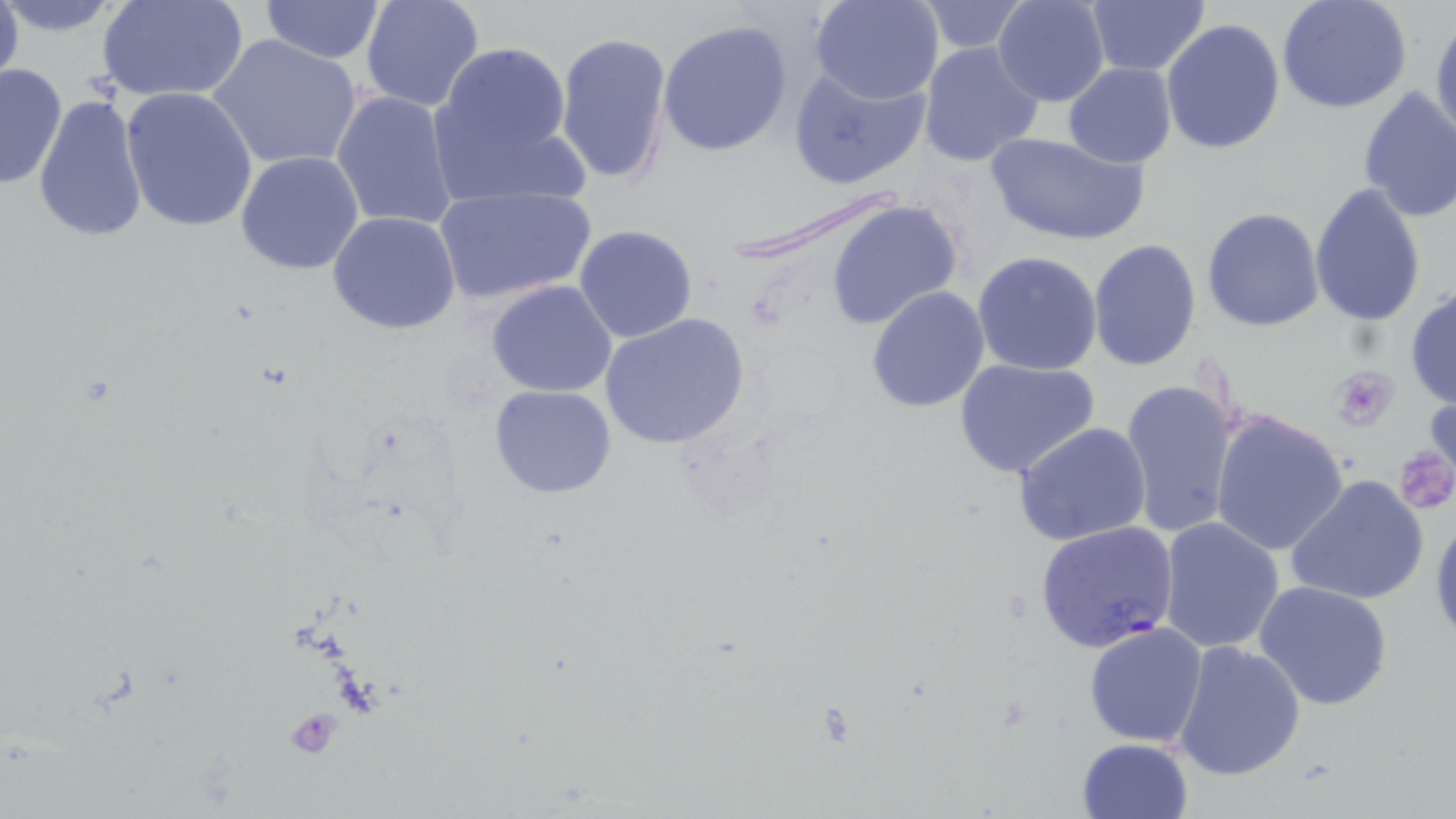

{
  "slide_level_diagnosis": "Plasmodium falciparum",
  "preparation": "thin blood film",
  "image_size": "1456×819 pixels",
  "platelet_locations": "approximate bounding boxes as (x1,y1)-(x2,y2) corner pairs in pixels: (1332,366)-(1398,431), (1394,444)-(1455,513), (286,706)-(343,758)",
  "magnification": "1000x",
  "uninfected_red_blood_cell_locations": "approximate bounding boxes as (x1,y1)-(x2,y2) corner pairs in pixels: (0,0)-(23,96), (0,0)-(127,34), (98,0)-(246,102), (360,0)-(487,112), (811,0)-(945,105), (993,0)-(1110,107), (1086,0)-(1211,75), (259,1)-(382,64), (915,1)-(1032,54), (1277,1)-(1412,114), (1430,16)-(1455,143), (1161,19)-(1287,156), (659,20)-(792,156), (554,30)-(673,190), (208,34)-(363,174), (436,41)-(572,161), (917,41)-(1045,168), (2,63)-(66,191), (1063,63)-(1177,167), (788,64)-(930,188), (1357,86)-(1456,225), (119,87)-(259,233), (332,90)-(459,231), (33,92)-(148,243), (438,108)-(590,210), (984,129)-(1148,246), (235,151)-(365,275), (1310,182)-(1427,327), (724,185)-(913,275), (433,186)-(597,306), (826,199)-(963,330), (1203,207)-(1324,332), (327,211)-(461,335), (575,224)-(698,344), (1088,238)-(1202,370), (973,250)-(1103,376), (486,280)-(618,399), (866,285)-(991,413), (1406,285)-(1456,409), (602,311)-(749,451), (954,359)-(1101,478), (1120,376)-(1243,538), (489,384)-(617,498), (1208,409)-(1351,557), (1012,422)-(1153,548), (1287,475)-(1431,609), (1430,511)-(1456,648), (1158,516)-(1286,655), (1254,581)-(1394,711), (1084,621)-(1208,748), (1172,638)-(1306,780), (1077,738)-(1196,819)",
  "modality": "light microscopy",
  "plasmodium_falciparum_infected_red_blood_cell_locations": "approximate bounding boxes as (x1,y1)-(x2,y2) corner pairs in pixels: (1036,521)-(1180,653)",
  "field_of_view": "single",
  "stain": "May-Grünwald-Giemsa"
}